Draw a bounding box around every malaria parasite, every leukocyte, and every artifact (stain precipitate or debris).
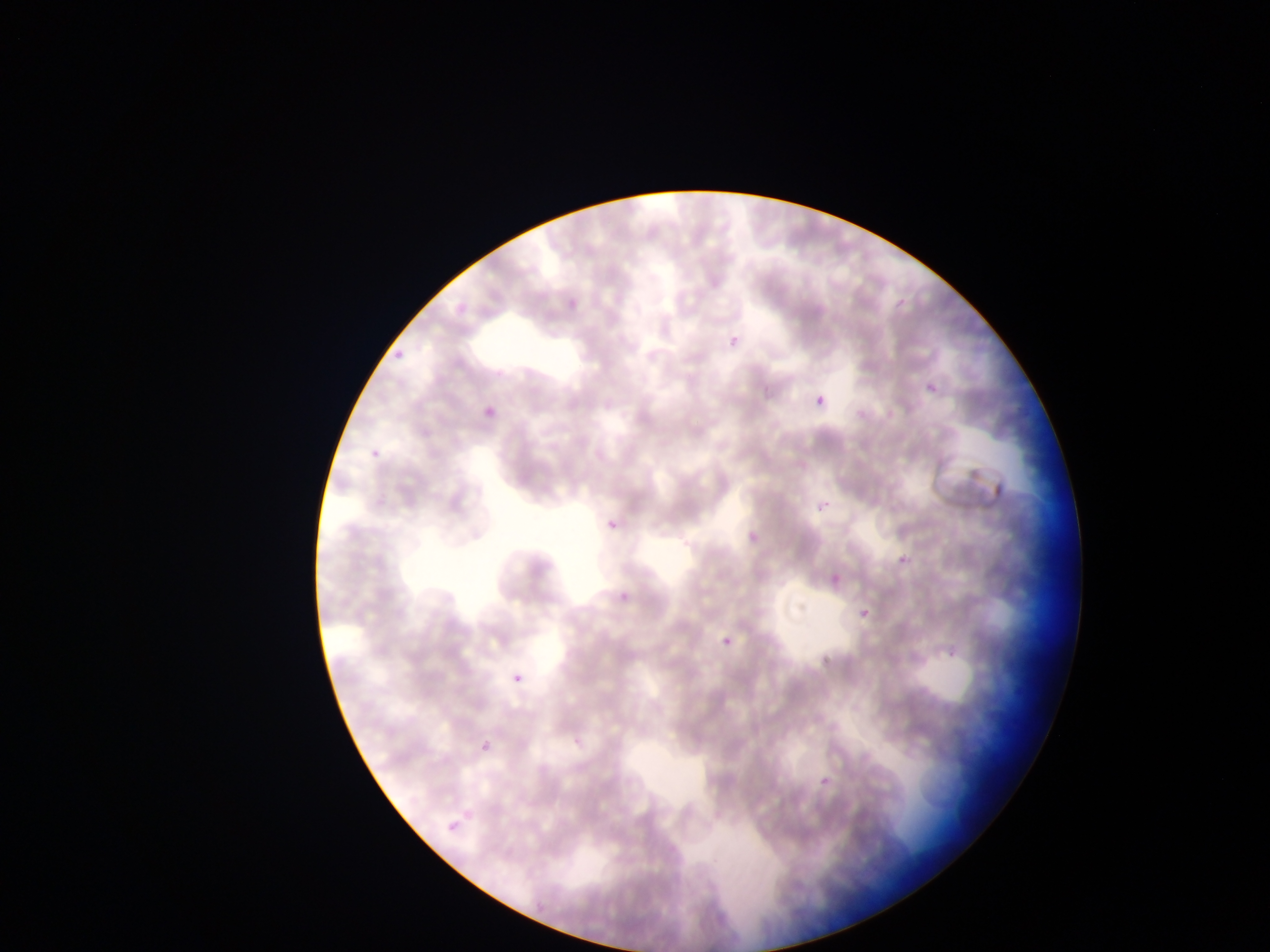
Approximate bounding boxes as (left, top, right, bottom) in pixels.
Malaria parasites: (565, 297, 580, 311), (445, 303, 471, 319), (728, 336, 739, 348), (388, 344, 409, 364), (928, 384, 937, 394), (816, 395, 824, 405), (480, 398, 494, 426), (417, 416, 440, 440), (364, 435, 386, 465), (815, 488, 834, 511), (745, 513, 771, 543), (607, 518, 620, 530), (825, 551, 855, 596), (898, 556, 908, 565), (611, 586, 636, 605), (860, 609, 870, 618), (723, 638, 732, 647), (511, 671, 524, 685), (480, 741, 490, 752), (813, 763, 829, 790), (445, 813, 462, 844).
No leukocytes observed.

Image is 1270×952 pixels. Sample from Ghana. Mobile-phone photograph taken through the microscope. Thin blood smear. One field of view.